Point out each malaria parasite.
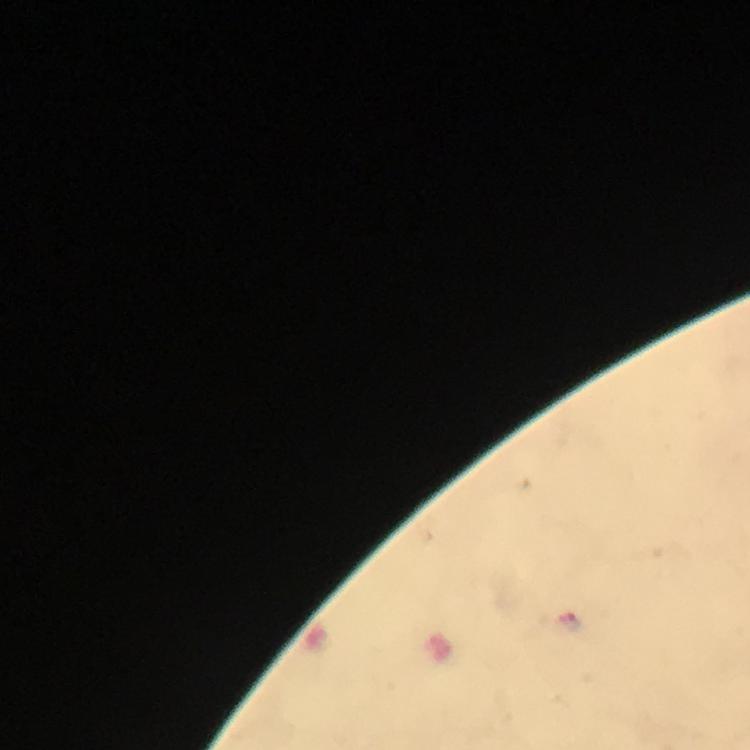

Approximate centers as {x, y} in pixels.
Malaria parasites: {568, 621}.

Summary:
  - Cropped from: a single field of view
  - Preparation: thick smear
  - Stain: Giemsa
  - Magnification: 100x
  - Image size: 750×750 pixels
  - Context: from a diagnostic examination for malaria
  - Immersion oil: applied
  - Capture: smartphone camera through the microscope